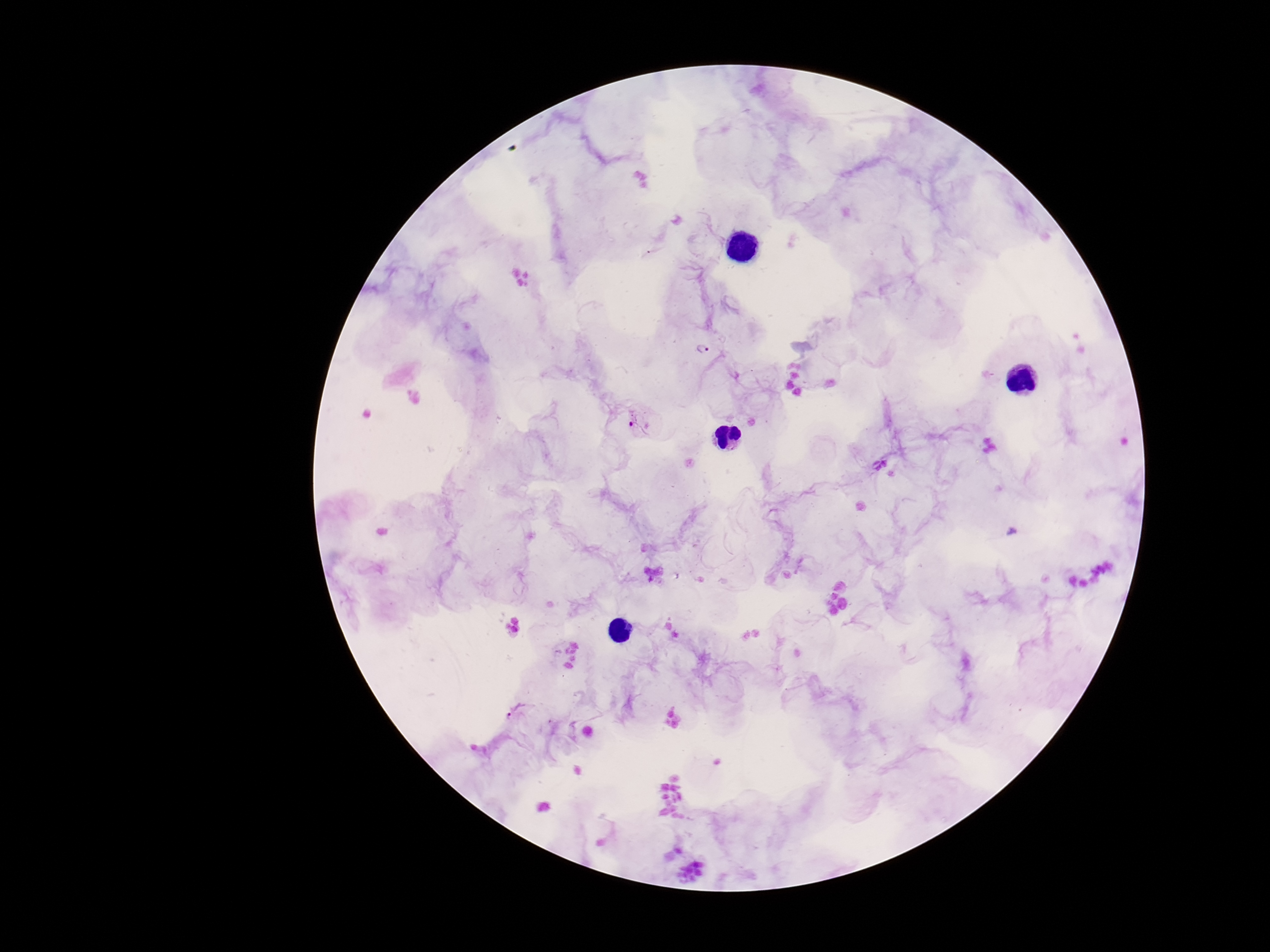

{
  "preparation": "thick blood film",
  "plasmodium_parasite_locations": "approximate object centers, in pixels from the top-left corner: (x=704, y=350), (x=637, y=426), (x=515, y=712)",
  "image_size": "1270×952 pixels",
  "field_of_view": "one from this slide",
  "patient_malaria_status": "infected",
  "capture": "smartphone camera through the microscope eyepiece",
  "magnification": "100x",
  "stain": "Giemsa"
}